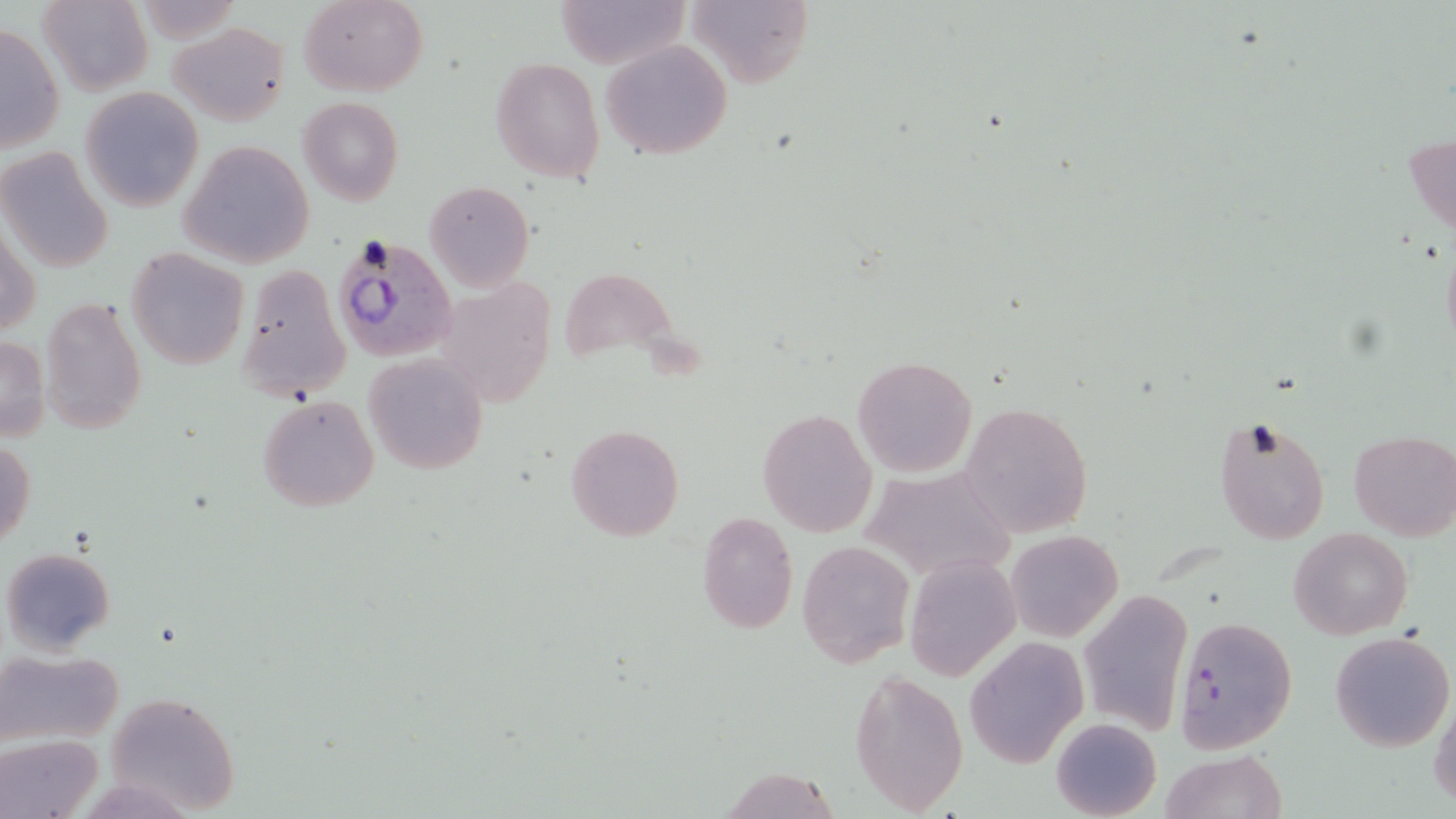

Summary:
  - Coordinate format: approximate bounding boxes as (x1,y1)-(x2,y2) corner pairs in pixels
  - Plasmodium falciparum-infected red blood cell locations: (328,231)-(459,363)
  - Uninfected red blood cell locations: (300,0)-(426,96), (556,0)-(689,69), (687,0)-(813,89), (39,1)-(152,96), (169,21)-(289,126), (0,22)-(65,155), (601,38)-(732,158), (490,57)-(607,185), (79,86)-(204,212), (298,97)-(404,207), (1404,132)-(1456,237), (178,140)-(315,268), (0,148)-(114,274), (423,178)-(535,293), (2,229)-(41,340), (1440,241)-(1456,357), (126,248)-(249,370), (236,263)-(349,401), (40,296)-(148,435), (0,335)-(51,442), (363,353)-(488,475), (852,354)-(978,477), (255,393)-(379,512), (959,401)-(1094,539), (758,407)-(877,539), (1212,414)-(1331,545), (565,424)-(685,543), (1349,431)-(1456,540), (0,437)-(36,547), (859,465)-(1015,583), (694,512)-(799,636), (1289,528)-(1413,640), (1007,530)-(1121,640), (796,539)-(916,667), (2,546)-(116,656), (903,554)-(1020,681), (1079,591)-(1193,736), (1173,615)-(1299,754), (1330,630)-(1455,752), (965,636)-(1090,768), (2,649)-(122,747), (849,668)-(970,816), (103,691)-(241,816), (1429,699)-(1456,808), (1051,718)-(1161,819), (2,735)-(101,819), (1158,749)-(1287,819), (716,765)-(842,819)
  - Slide-level diagnosis: Plasmodium falciparum
  - Magnification: 1000x
  - Modality: light microscopy
  - Image size: 1456×819 pixels
  - Preparation: thin blood smear
  - Stain: May-Grünwald-Giemsa
  - Field of view: one of a larger specimen